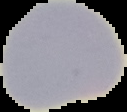
Summary:
  - Preparation: thin blood film
  - Image size: 127×112 pixels
  - Image type: segmented cell region with the area outside set to black
  - Malaria status: uninfected